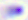

Summary:
  - Modality: photomicrograph
  - Identification: Toxoplasma gondii
  - Magnification: 400x